Report the malaria status of this cell.
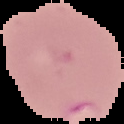

Parasitized.

preparation = thin blood smear
image size = 124×124 pixels
image type = segmented cell region on a black background